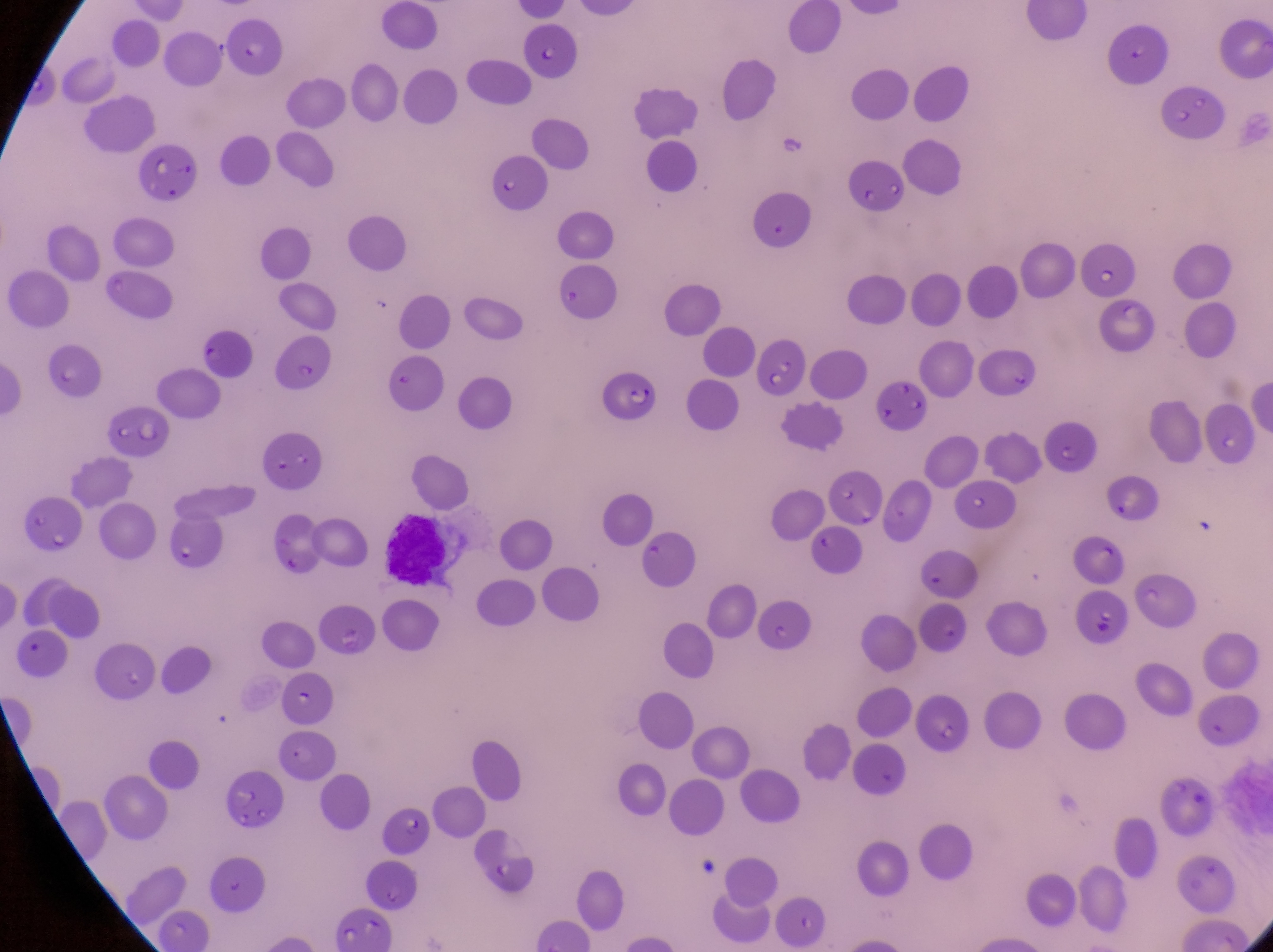
Approximate bounding boxes as (left, top, right, bottom) in pixels.
Summary:
  - Parasitised red blood cell locations: (609, 360, 659, 423), (107, 407, 174, 460), (22, 500, 79, 553), (379, 507, 467, 590)
  - Artifact (platelet-like body, stain precipitate, or debris) locations: (771, 125, 818, 167)
  - Capture: smartphone photograph through the eyepiece of an Olympus CX-23 microscope
  - Field of view: single
  - Preparation: thin blood smear
  - Country: Uganda
  - Image size: 1273×952 pixels
  - Magnification: 1000x